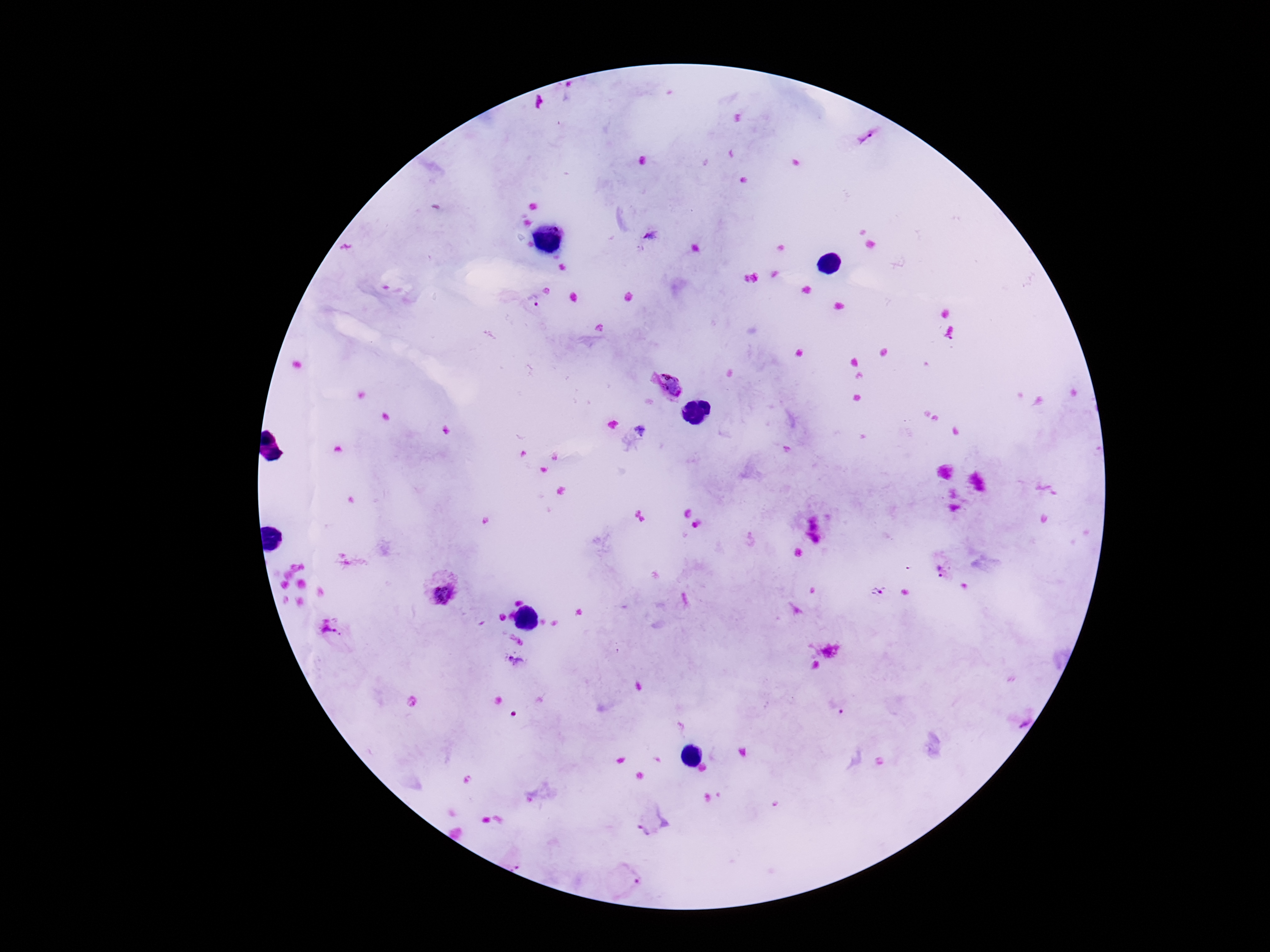
Approximate centers as {x, y} in pixels. Plasmodium parasite locations: {867, 135}, {650, 234}, {533, 299}, {666, 385}, {940, 573}, {438, 587}, {878, 591}, {334, 634}, {516, 662}, {653, 822}, {630, 878}. Smartphone photograph taken through the microscope eyepiece. Thick blood smear. 100x magnification. Giemsa stain. Image is 1270×952 pixels. One field from this slide. Patient malaria status: infected.